Classify this cell by malaria status.
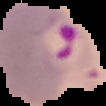
Parasitized.

From a thin blood film. Cell region segmented out of the field of view; the surrounding area is masked to black. Image is 106×106 pixels.